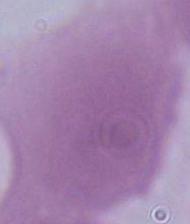
Micrograph. An erythrocyte is seen. Captured at 1000x magnification.